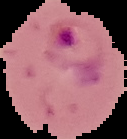

malaria status = parasitized
preparation = thin blood film
image type = segmented cell region with the area outside set to black
image size = 127×139 pixels